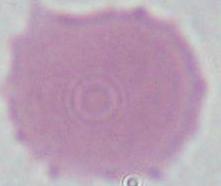
{
  "identification": "erythrocyte",
  "modality": "photomicrograph",
  "magnification": "1000x"
}